Identify the parasite.
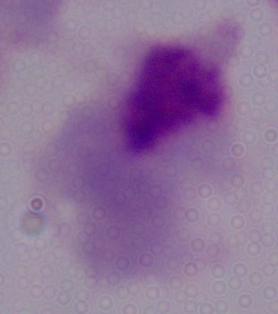

A trichomonad.

Summary:
  - Magnification: 1000x
  - Modality: micrograph